Identify the cell.
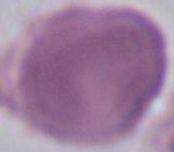

An erythrocyte.

Summary:
  - Modality: micrograph
  - Magnification: 1000x